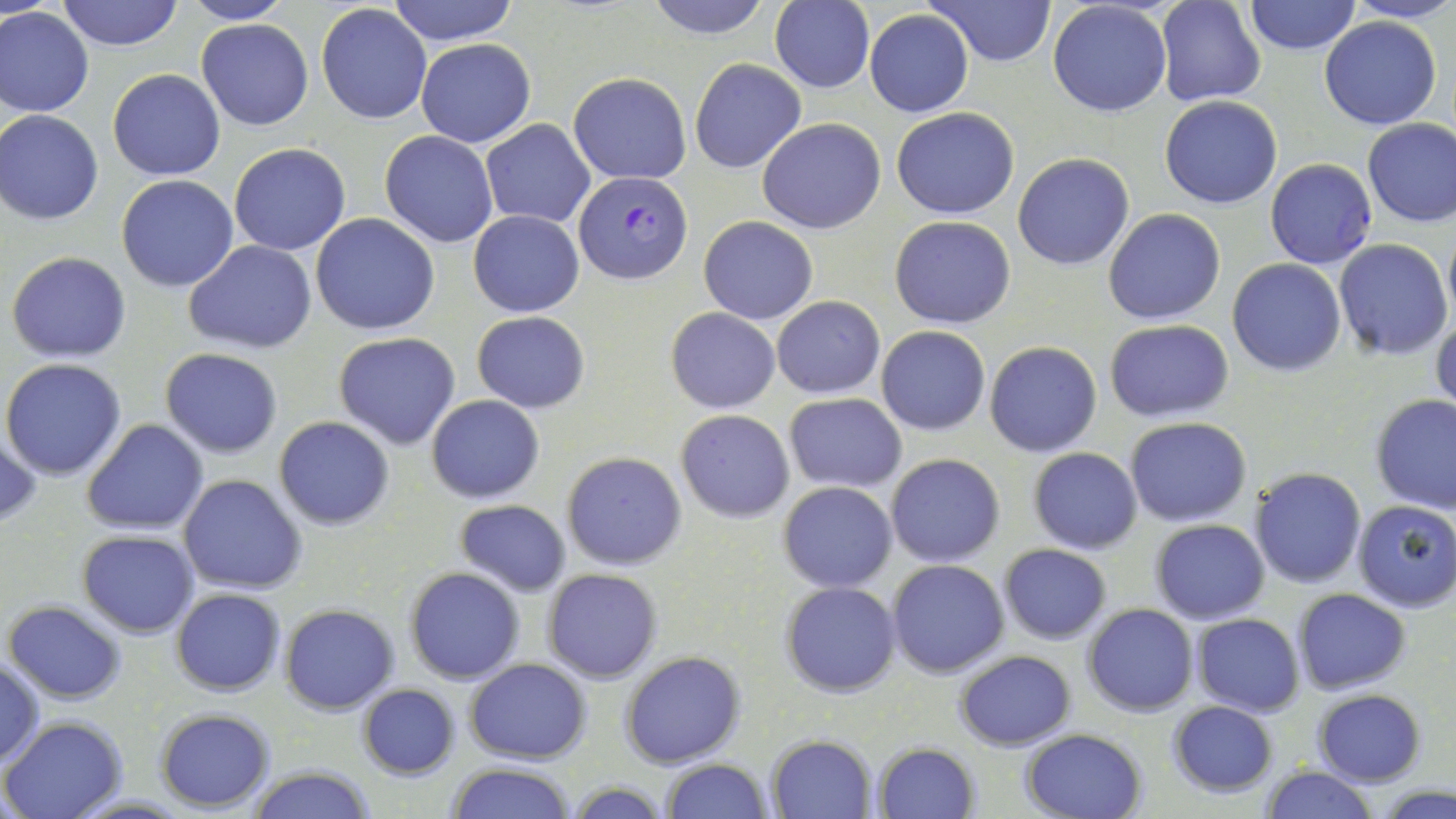
Summary:
  - Coordinate format: approximate bounding boxes as (x1, y1, x2, y2) in pixels
  - Uninfected red blood cell locations: (57, 0, 182, 51), (181, 0, 298, 24), (387, 0, 519, 47), (641, 0, 776, 40), (926, 0, 1058, 68), (1157, 0, 1266, 107), (1343, 0, 1456, 24), (770, 1, 874, 93), (1047, 1, 1173, 117), (1243, 1, 1360, 55), (316, 3, 432, 126), (0, 7, 94, 118), (865, 10, 974, 119), (1318, 16, 1441, 130), (196, 19, 315, 132), (415, 38, 535, 148), (690, 59, 806, 174), (108, 68, 226, 181), (567, 70, 691, 184), (1158, 96, 1283, 210), (891, 106, 1019, 219), (0, 109, 106, 225), (757, 117, 886, 234), (1361, 117, 1456, 228), (481, 120, 594, 229), (380, 130, 498, 248), (228, 142, 352, 255), (1013, 153, 1134, 271), (1264, 159, 1378, 269), (116, 174, 240, 292), (1102, 208, 1227, 325), (468, 210, 583, 317), (310, 213, 440, 336), (890, 215, 1017, 329), (699, 216, 818, 324), (1443, 230, 1456, 321), (1334, 239, 1453, 359), (183, 240, 316, 352), (6, 251, 132, 362), (1227, 259, 1346, 376), (771, 295, 885, 398), (666, 308, 779, 413), (471, 310, 591, 412), (1431, 310, 1456, 418), (1104, 319, 1234, 422), (876, 326, 990, 435), (333, 332, 461, 450), (984, 341, 1101, 457), (161, 348, 284, 459), (1, 358, 127, 481), (785, 393, 907, 491), (427, 394, 544, 503), (1371, 394, 1456, 514), (675, 409, 794, 523), (274, 415, 396, 530), (1124, 418, 1252, 527), (81, 419, 208, 535), (0, 428, 47, 531), (1028, 447, 1144, 554), (562, 451, 687, 570), (885, 454, 1005, 568), (1249, 467, 1365, 589), (177, 474, 308, 594), (777, 480, 898, 593), (454, 499, 572, 595), (1352, 500, 1456, 612), (1151, 520, 1270, 624), (77, 530, 199, 637), (998, 544, 1112, 644), (887, 559, 1010, 678), (405, 567, 525, 684), (541, 569, 663, 683), (780, 582, 900, 698), (1293, 588, 1411, 695), (170, 589, 286, 695), (3, 600, 127, 704), (280, 603, 398, 715), (1082, 603, 1197, 717), (1191, 613, 1305, 716), (954, 649, 1074, 749), (620, 650, 744, 768), (0, 656, 45, 767), (465, 659, 591, 764), (356, 684, 461, 779), (1313, 689, 1426, 785), (1165, 701, 1279, 798), (155, 708, 275, 811), (1, 715, 129, 818), (1020, 729, 1147, 819), (766, 734, 876, 817), (871, 743, 980, 819), (660, 758, 776, 818), (444, 763, 577, 819), (245, 764, 375, 819), (1258, 765, 1378, 819), (562, 780, 672, 818), (1374, 784, 1456, 818)
  - Plasmodium falciparum-infected red blood cell locations: (577, 172, 691, 282)
  - Slide-level diagnosis: Plasmodium falciparum
  - Stain: May-Grünwald-Giemsa
  - Preparation: thin blood smear
  - Modality: light microscopy
  - Magnification: 1000x
  - Image size: 1456×819 pixels
  - Field of view: one of a larger specimen